Assess this cell for malaria.
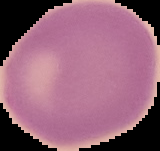
It is uninfected.

preparation: thin blood film
image_size: 160×151 pixels
image_type: segmented cell region with the area outside set to black